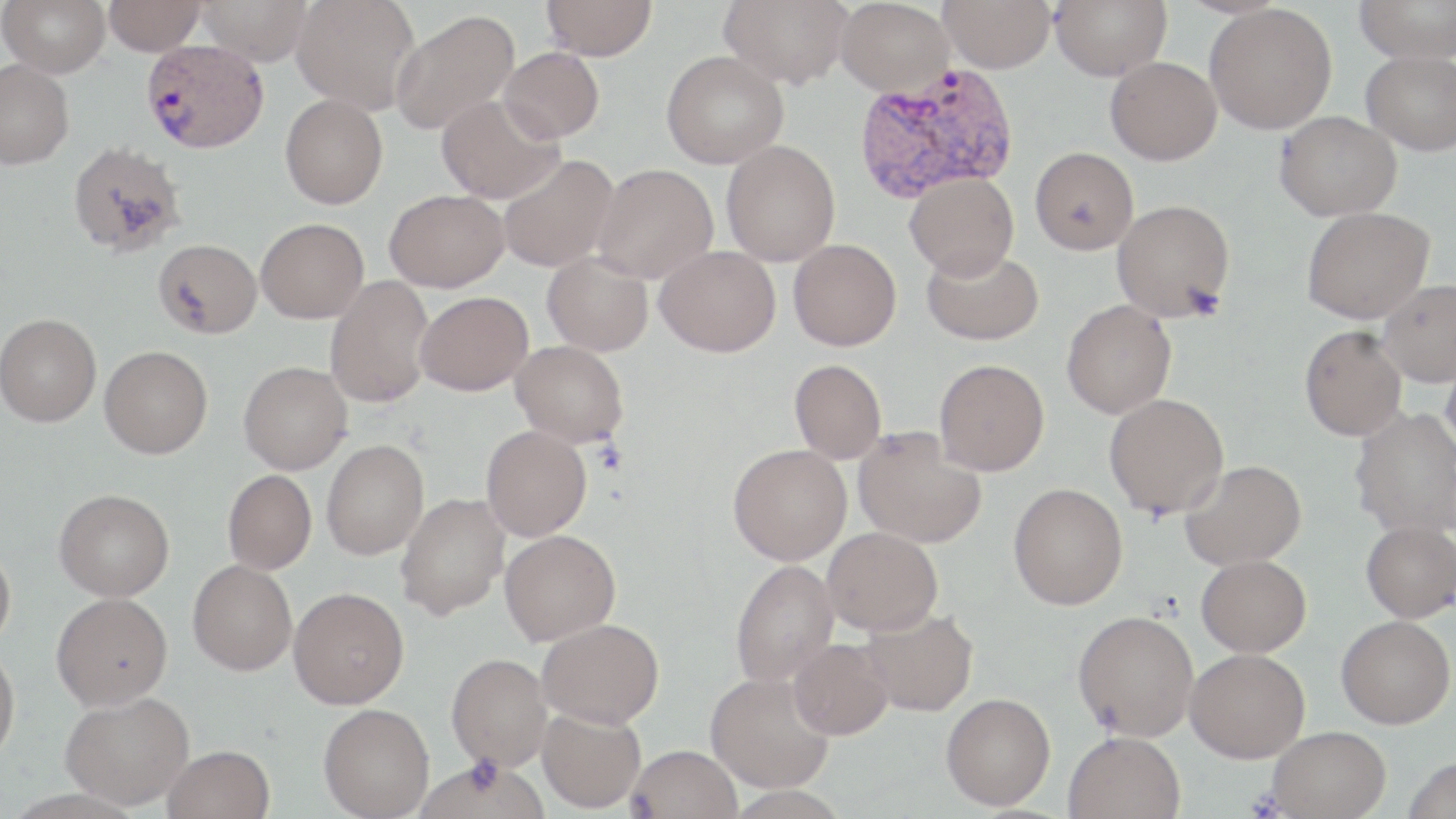

Summary:
  - Coordinate format: approximate bounding boxes as (x1,y1)-(x2,y2) corner pairs in pixels
  - Plasmodium vivax-infected red blood cell locations: (141,39)-(268,153), (853,64)-(1019,204)
  - Uninfected red blood cell locations: (1,0)-(110,77), (104,0)-(206,56), (195,0)-(313,66), (292,0)-(420,113), (541,0)-(657,61), (720,0)-(853,88), (836,0)-(954,95), (939,0)-(1056,73), (1050,0)-(1171,80), (1354,0)-(1456,63), (1204,3)-(1337,135), (389,9)-(519,135), (499,47)-(604,143), (1361,50)-(1456,155), (661,51)-(788,169), (1105,56)-(1222,165), (0,59)-(74,169), (280,94)-(387,209), (436,95)-(563,204), (1274,110)-(1401,221), (67,140)-(185,257), (721,140)-(840,266), (1029,146)-(1138,255), (497,154)-(619,273), (592,163)-(718,282), (905,171)-(1019,280), (384,189)-(509,292), (1112,199)-(1235,321), (1301,206)-(1434,324), (255,218)-(369,323), (153,239)-(261,338), (788,239)-(901,351), (655,245)-(780,356), (921,246)-(1044,345), (542,252)-(653,356), (324,276)-(436,408), (1378,279)-(1456,386), (415,291)-(533,396), (1061,300)-(1176,419), (0,313)-(102,426), (1298,325)-(1406,441), (511,340)-(629,447), (99,345)-(212,458), (1440,352)-(1456,459), (934,359)-(1049,475), (789,360)-(887,463), (238,361)-(352,474), (1104,393)-(1229,519), (1350,407)-(1456,539), (481,425)-(592,541), (854,427)-(987,549), (321,439)-(429,560), (728,444)-(851,565), (1180,459)-(1306,570), (222,470)-(316,574), (1008,482)-(1128,610), (54,488)-(174,601), (396,492)-(510,620), (1361,520)-(1456,622), (822,527)-(943,635), (499,529)-(620,645), (0,542)-(16,651), (1196,554)-(1311,657), (188,560)-(297,675), (730,560)-(839,688), (289,587)-(409,709), (51,592)-(173,710), (860,607)-(979,716), (1073,610)-(1199,741), (1336,615)-(1455,729), (537,618)-(664,729), (788,638)-(894,740), (0,644)-(20,765), (1185,648)-(1310,763), (447,653)-(553,770), (705,671)-(836,793), (60,691)-(195,809), (941,692)-(1056,810), (318,703)-(434,818), (537,707)-(646,813), (1266,725)-(1391,818), (1063,730)-(1186,819), (163,744)-(275,819), (628,744)-(742,819), (1403,755)-(1456,819)
  - Platelet locations: (1182,284)-(1226,320)
  - Slide-level diagnosis: Plasmodium vivax
  - Modality: light microscopy
  - Stain: May-Grünwald-Giemsa
  - Field of view: one of a larger specimen
  - Preparation: thin blood smear
  - Image size: 1456×819 pixels
  - Magnification: 1000x